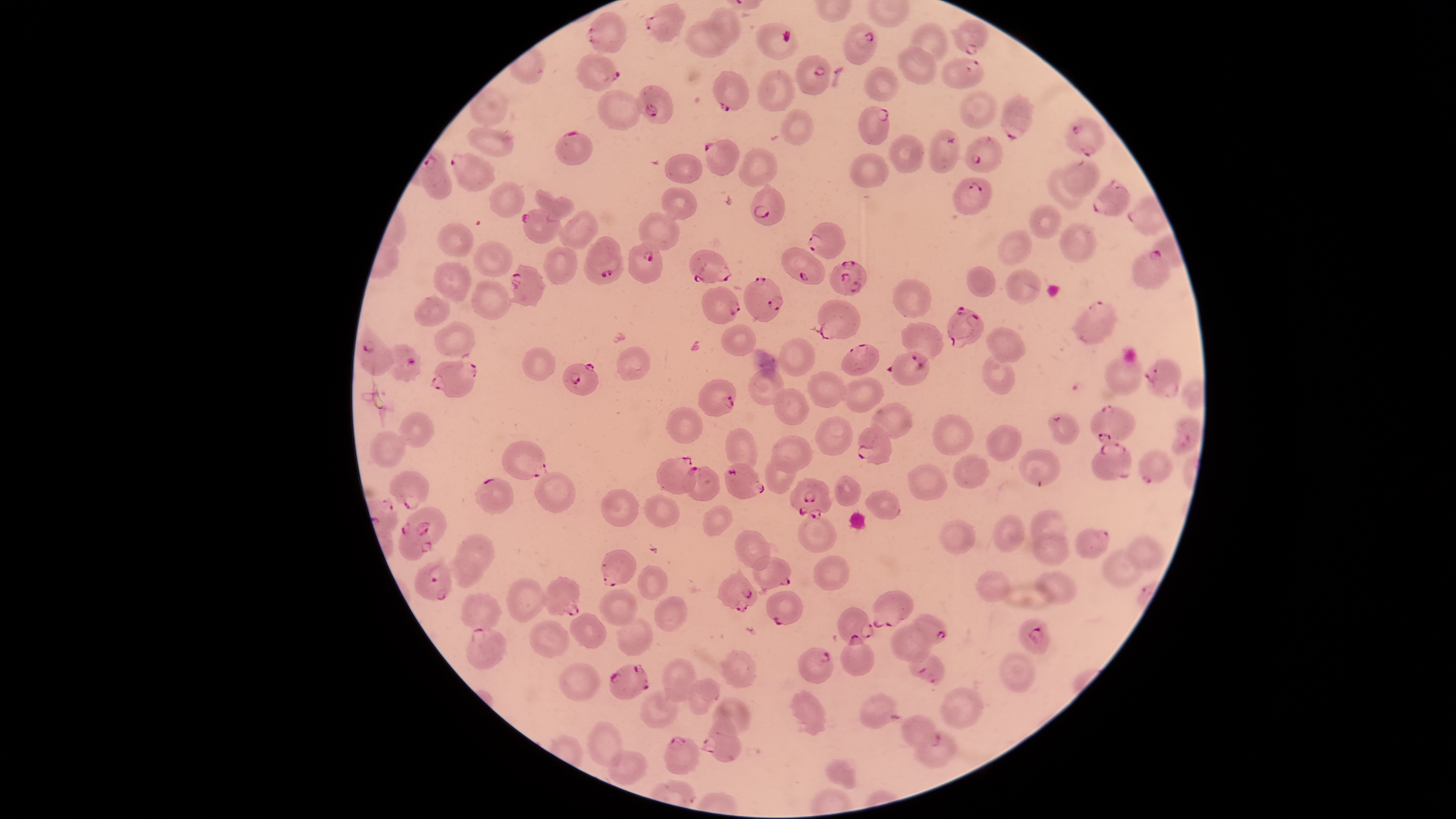

field of view = single
parasitized red blood cells = approximate bounding boxes, in pixels from the top-left corner: (left=645, top=3, right=684, bottom=42), (left=585, top=12, right=626, bottom=53), (left=950, top=19, right=988, bottom=55), (left=844, top=22, right=877, bottom=65), (left=578, top=53, right=619, bottom=91), (left=796, top=55, right=830, bottom=94), (left=940, top=57, right=983, bottom=89), (left=711, top=71, right=749, bottom=112), (left=636, top=84, right=672, bottom=125), (left=1001, top=93, right=1032, bottom=141), (left=859, top=107, right=889, bottom=145), (left=1064, top=118, right=1103, bottom=157), (left=929, top=128, right=960, bottom=174), (left=555, top=130, right=592, bottom=165), (left=965, top=136, right=1002, bottom=173), (left=704, top=139, right=738, bottom=175), (left=449, top=152, right=496, bottom=193), (left=419, top=155, right=452, bottom=199), (left=953, top=177, right=992, bottom=215), (left=1092, top=179, right=1129, bottom=217), (left=751, top=183, right=785, bottom=226), (left=521, top=209, right=562, bottom=244), (left=806, top=220, right=845, bottom=260), (left=587, top=237, right=621, bottom=277), (left=627, top=242, right=662, bottom=283), (left=781, top=247, right=826, bottom=284), (left=689, top=249, right=732, bottom=283), (left=1131, top=251, right=1171, bottom=289), (left=829, top=260, right=865, bottom=296), (left=509, top=265, right=546, bottom=306), (left=743, top=276, right=783, bottom=323), (left=702, top=287, right=740, bottom=322), (left=811, top=299, right=860, bottom=339), (left=1071, top=300, right=1117, bottom=344), (left=947, top=306, right=984, bottom=349), (left=901, top=321, right=943, bottom=366), (left=355, top=324, right=395, bottom=377), (left=384, top=344, right=421, bottom=381), (left=841, top=344, right=879, bottom=375), (left=885, top=352, right=929, bottom=386), (left=1144, top=357, right=1182, bottom=397), (left=430, top=360, right=476, bottom=398), (left=564, top=363, right=598, bottom=395), (left=698, top=379, right=737, bottom=416), (left=1089, top=404, right=1136, bottom=444), (left=1047, top=413, right=1080, bottom=445), (left=1171, top=416, right=1202, bottom=454), (left=857, top=425, right=891, bottom=466), (left=503, top=441, right=548, bottom=480), (left=1090, top=441, right=1131, bottom=481), (left=1139, top=450, right=1173, bottom=485), (left=656, top=456, right=697, bottom=495), (left=722, top=463, right=765, bottom=499), (left=684, top=466, right=720, bottom=501), (left=389, top=471, right=429, bottom=509), (left=790, top=477, right=833, bottom=520), (left=476, top=478, right=514, bottom=516), (left=401, top=507, right=447, bottom=552), (left=399, top=521, right=430, bottom=561), (left=1076, top=528, right=1109, bottom=559), (left=601, top=549, right=637, bottom=586), (left=752, top=555, right=791, bottom=595), (left=415, top=557, right=452, bottom=600), (left=718, top=568, right=759, bottom=613), (left=541, top=576, right=580, bottom=616), (left=766, top=591, right=804, bottom=625), (left=871, top=591, right=914, bottom=628), (left=838, top=607, right=874, bottom=644), (left=910, top=614, right=948, bottom=645), (left=1018, top=618, right=1050, bottom=655), (left=466, top=627, right=505, bottom=668), (left=842, top=634, right=875, bottom=676), (left=799, top=647, right=834, bottom=683), (left=908, top=648, right=944, bottom=688), (left=610, top=664, right=649, bottom=699), (left=859, top=693, right=903, bottom=729), (left=700, top=713, right=742, bottom=763), (left=900, top=715, right=940, bottom=752), (left=664, top=737, right=700, bottom=774)
presence = malaria parasites detected
visible region = circular
species = Plasmodium falciparum
uninfected red blood cells = approximate bounding boxes, in pixels from the top-left corner: (left=708, top=8, right=742, bottom=46), (left=686, top=20, right=731, bottom=56), (left=756, top=23, right=796, bottom=59), (left=907, top=23, right=947, bottom=64), (left=897, top=46, right=936, bottom=84), (left=864, top=67, right=898, bottom=100), (left=758, top=69, right=796, bottom=113), (left=469, top=87, right=508, bottom=125), (left=598, top=90, right=642, bottom=129), (left=959, top=91, right=997, bottom=128), (left=781, top=109, right=814, bottom=145), (left=467, top=127, right=513, bottom=157), (left=889, top=136, right=923, bottom=174), (left=739, top=148, right=777, bottom=188), (left=850, top=152, right=887, bottom=188), (left=664, top=154, right=702, bottom=183), (left=1058, top=161, right=1100, bottom=197), (left=1045, top=169, right=1081, bottom=209), (left=490, top=182, right=524, bottom=219), (left=661, top=188, right=697, bottom=219), (left=534, top=190, right=575, bottom=220), (left=1029, top=206, right=1061, bottom=238), (left=558, top=211, right=598, bottom=251), (left=639, top=213, right=679, bottom=251), (left=438, top=222, right=474, bottom=256), (left=1058, top=222, right=1097, bottom=262), (left=997, top=229, right=1031, bottom=265), (left=474, top=241, right=512, bottom=275), (left=544, top=245, right=576, bottom=284), (left=434, top=261, right=472, bottom=301), (left=966, top=266, right=996, bottom=297), (left=1005, top=268, right=1041, bottom=304), (left=472, top=279, right=510, bottom=319), (left=892, top=279, right=931, bottom=317), (left=415, top=297, right=450, bottom=326), (left=434, top=322, right=476, bottom=356), (left=720, top=325, right=756, bottom=357), (left=987, top=326, right=1027, bottom=362), (left=780, top=337, right=815, bottom=376), (left=616, top=346, right=651, bottom=382), (left=522, top=347, right=555, bottom=381), (left=982, top=353, right=1016, bottom=394), (left=1104, top=356, right=1142, bottom=395), (left=749, top=367, right=784, bottom=404), (left=806, top=371, right=847, bottom=407), (left=840, top=377, right=883, bottom=412), (left=773, top=389, right=809, bottom=425), (left=872, top=403, right=914, bottom=438), (left=666, top=407, right=703, bottom=444), (left=398, top=412, right=434, bottom=448), (left=930, top=414, right=973, bottom=456), (left=815, top=416, right=854, bottom=457), (left=985, top=425, right=1023, bottom=461), (left=725, top=428, right=757, bottom=471), (left=370, top=431, right=406, bottom=469), (left=772, top=434, right=813, bottom=471), (left=1020, top=450, right=1061, bottom=486), (left=952, top=453, right=989, bottom=488), (left=765, top=455, right=797, bottom=495), (left=908, top=463, right=948, bottom=499), (left=534, top=473, right=575, bottom=512), (left=834, top=475, right=860, bottom=506), (left=600, top=489, right=640, bottom=527), (left=865, top=490, right=901, bottom=520), (left=644, top=495, right=680, bottom=526), (left=703, top=504, right=732, bottom=537), (left=1030, top=510, right=1067, bottom=549), (left=992, top=513, right=1026, bottom=553), (left=798, top=516, right=836, bottom=551), (left=940, top=519, right=974, bottom=555), (left=733, top=530, right=771, bottom=571), (left=1033, top=531, right=1069, bottom=565), (left=456, top=533, right=494, bottom=574), (left=1125, top=535, right=1165, bottom=572), (left=1102, top=549, right=1145, bottom=589), (left=449, top=552, right=484, bottom=589), (left=814, top=557, right=850, bottom=589), (left=638, top=566, right=668, bottom=600), (left=976, top=571, right=1010, bottom=602), (left=1035, top=571, right=1076, bottom=603), (left=506, top=578, right=548, bottom=622), (left=599, top=589, right=637, bottom=625), (left=460, top=592, right=502, bottom=632), (left=654, top=595, right=687, bottom=632), (left=570, top=612, right=605, bottom=649), (left=618, top=616, right=654, bottom=656), (left=530, top=619, right=568, bottom=656), (left=891, top=626, right=931, bottom=661), (left=719, top=650, right=756, bottom=690), (left=1000, top=653, right=1037, bottom=692), (left=663, top=659, right=697, bottom=702), (left=559, top=663, right=601, bottom=700), (left=688, top=679, right=719, bottom=715), (left=640, top=688, right=679, bottom=728), (left=940, top=688, right=981, bottom=727), (left=791, top=689, right=825, bottom=735), (left=713, top=695, right=750, bottom=736), (left=588, top=722, right=624, bottom=767), (left=915, top=731, right=956, bottom=767), (left=608, top=750, right=647, bottom=785), (left=827, top=760, right=856, bottom=790)
image size = 1456×819 pixels
stain = Giemsa
preparation = thin blood film
capture = smartphone photograph through the microscope eyepiece